Point out each Plasmodium parasite.
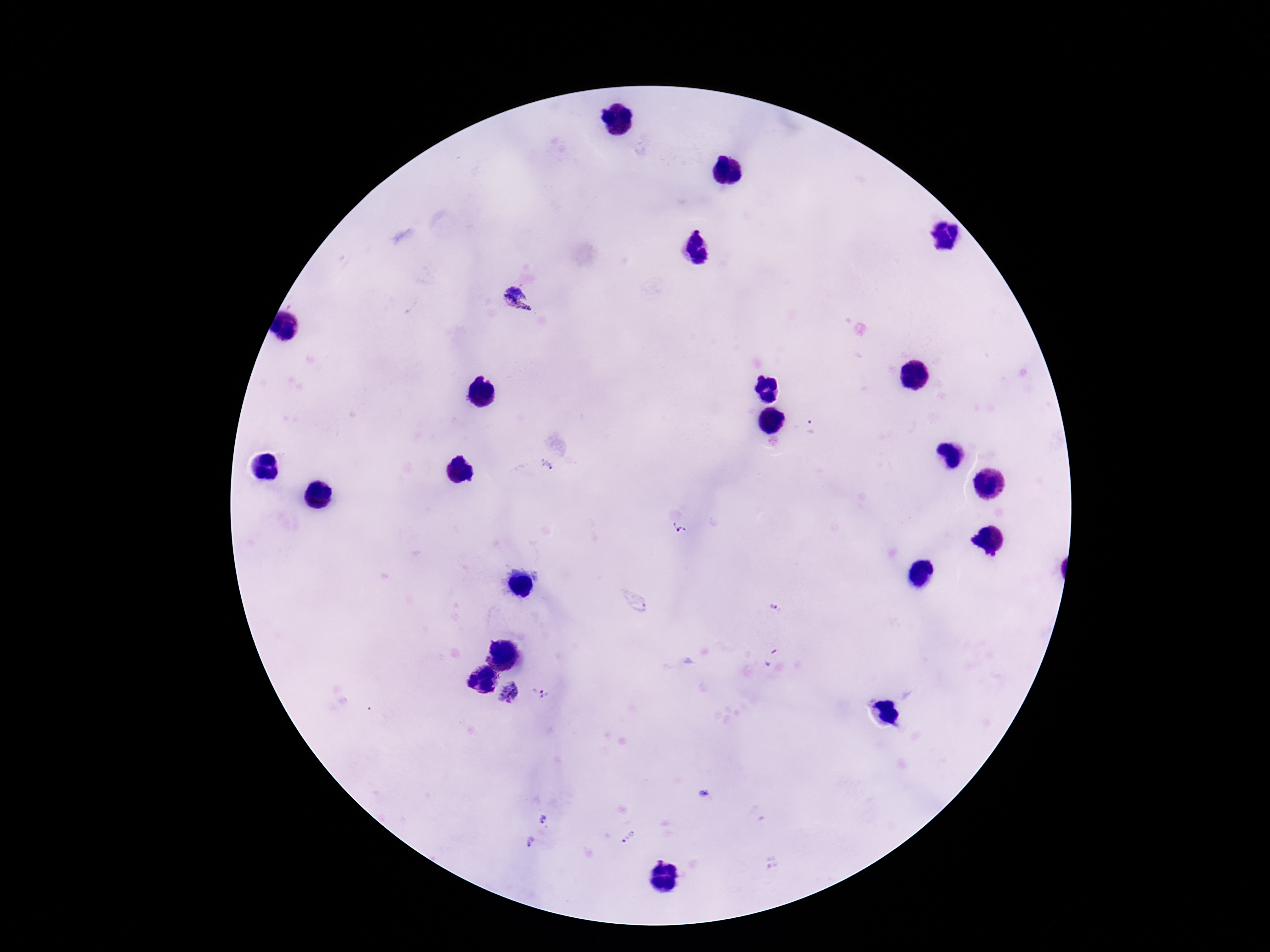
Approximate centers as (x, y) in pixels.
Plasmodium parasites: (520, 301), (812, 426), (548, 465), (681, 525), (776, 609), (770, 655), (508, 693), (541, 695), (545, 820), (629, 837), (530, 843).

Patient malaria status: infected. Single field of view. Image is 1270×952 pixels. 100x magnification. Thick blood film. Giemsa-stained preparation. Smartphone photograph taken through the microscope eyepiece.